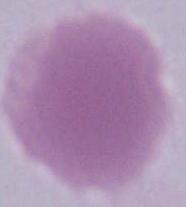

Summary:
  - Identification: red blood cell
  - Modality: photomicrograph
  - Magnification: 1000x